Locate every Plasmodium parasite.
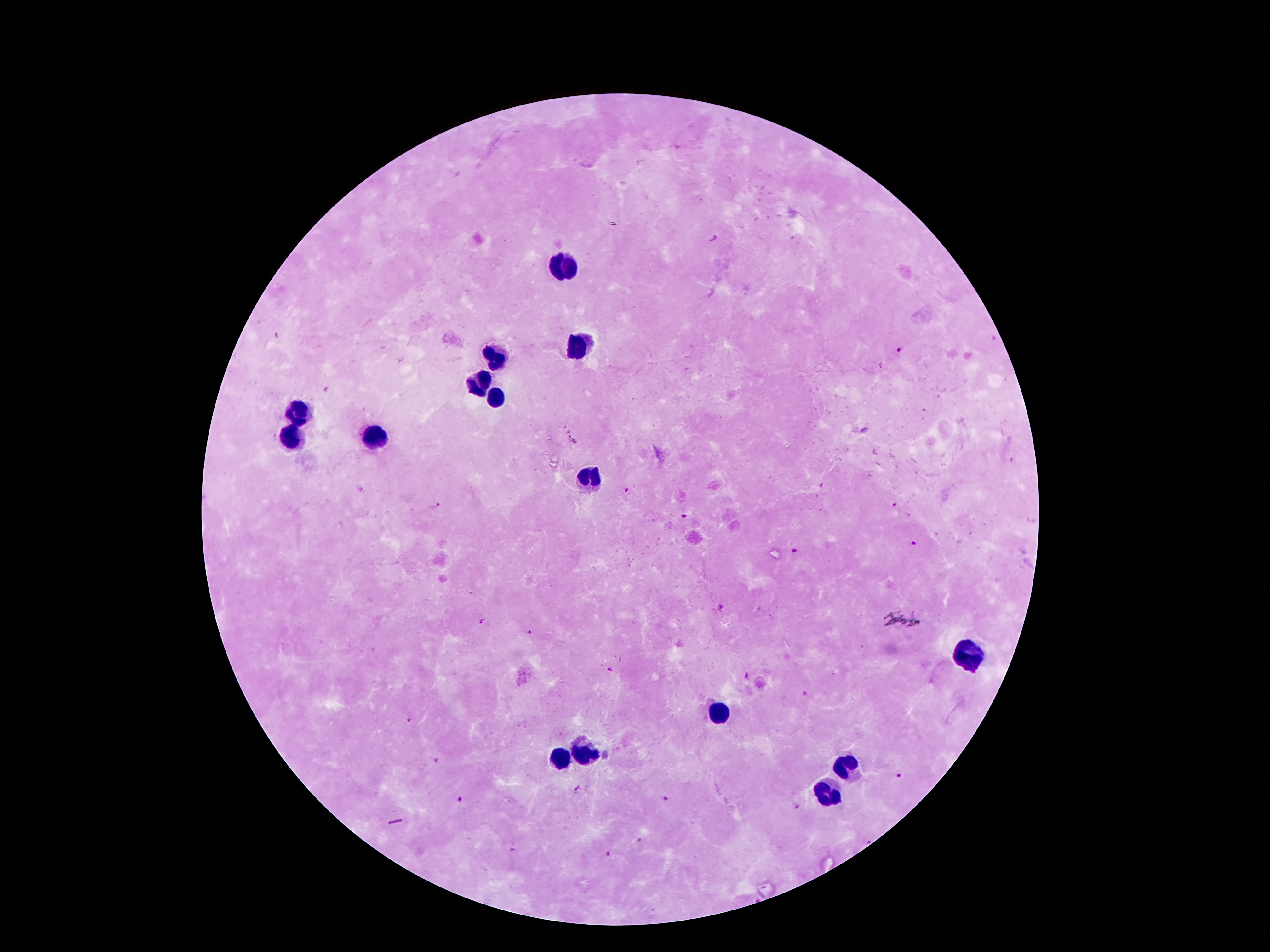

Approximate centers as {x, y} in pixels.
Plasmodium parasites: {711, 238}, {900, 351}, {823, 484}, {625, 489}, {436, 505}, {894, 505}, {683, 517}, {914, 543}, {793, 549}, {721, 606}, {483, 621}, {529, 632}, {611, 671}, {746, 676}, {803, 695}, {410, 719}, {438, 761}, {899, 775}, {577, 789}, {460, 799}, {664, 800}, {797, 807}, {867, 841}, {514, 850}, {605, 853}.

leukocyte locations = {561, 266}, {583, 342}, {493, 361}, {477, 382}, {495, 398}, {298, 409}, {294, 434}, {371, 436}, {586, 476}, {968, 657}, {722, 713}, {584, 753}, {558, 762}, {850, 766}, {831, 793}
preparation = thick blood film
magnification = 100x
stain = Giemsa
patient malaria status = infected with Plasmodium falciparum
capture = smartphone camera through the microscope eyepiece
image size = 1270×952 pixels
field of view = single